Comment on the morphology of the erythrocytes.
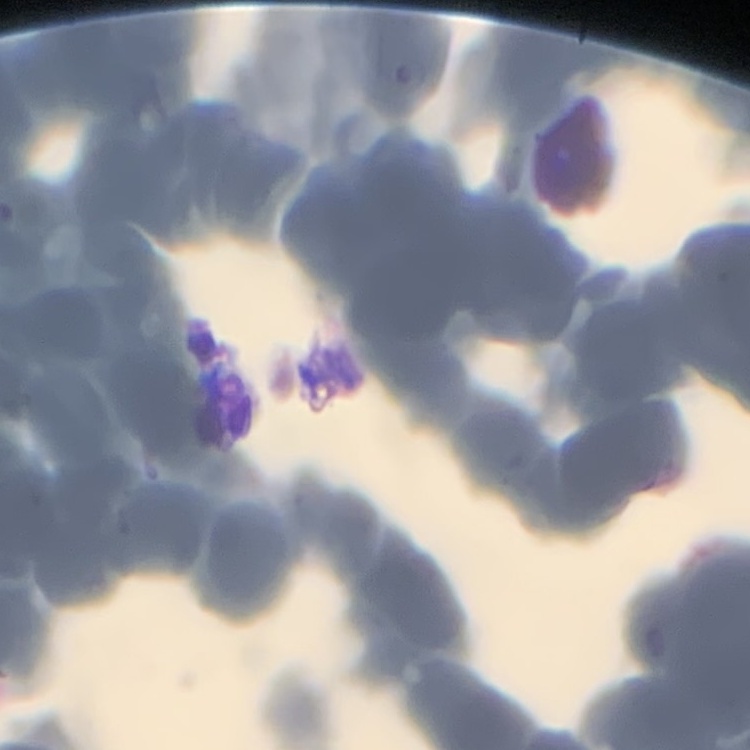
They show rouleaux formation.

Square crop of a larger photomicrograph. Stained with either Field's or Giemsa. Thin peripheral smear.